Identify the parasite.
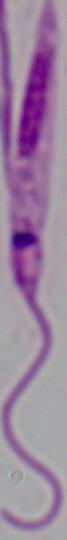

This is Leishmania.

modality = photomicrograph
magnification = 1000x